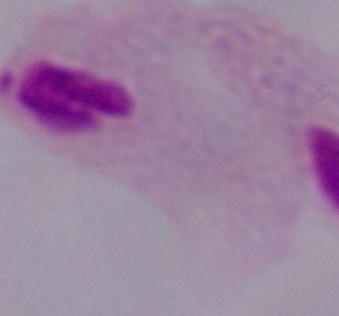

magnification: 1000x
modality: photomicrograph
identification: trichomonad